Comment on the morphology of the red blood cells.
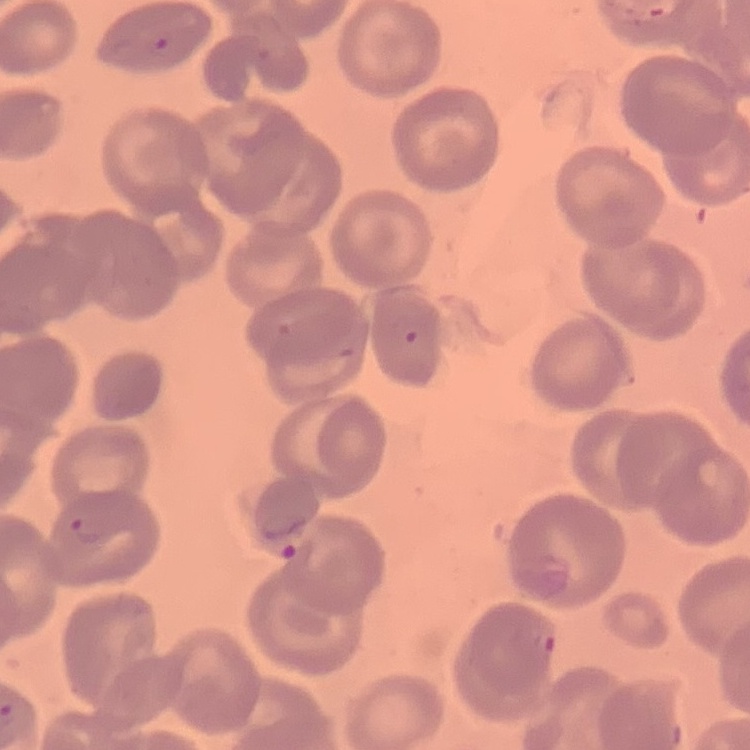

No rouleaux formation.

preparation = thin peripheral smear
stain = Field's or Giemsa
image type = one tile cut from a larger photomicrograph